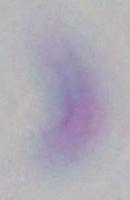
1000x magnification. Photomicrograph. Toxoplasma gondii is shown.